State which parasite is depicted.
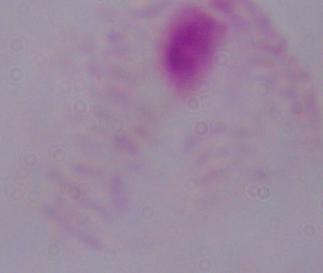

This is a trichomonad.

Summary:
  - Modality: photomicrograph
  - Magnification: 1000x